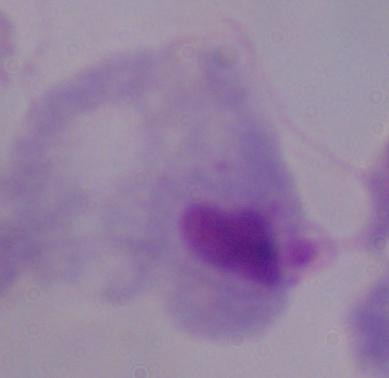

{
  "modality": "photomicrograph",
  "identification": "trichomonad",
  "magnification": "1000x"
}